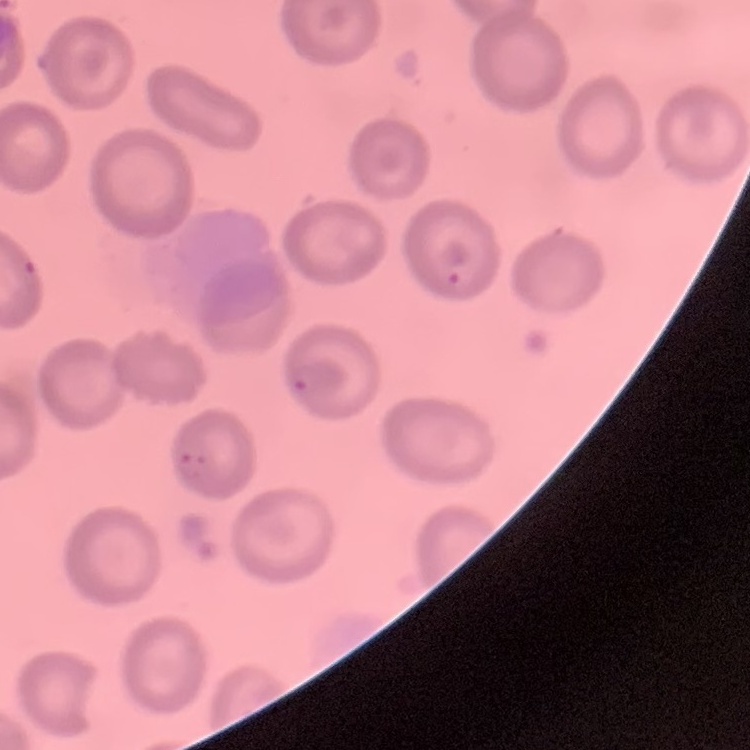
red blood cell morphology = no rouleaux formation
image type = one tile cut from a larger photomicrograph
preparation = thin blood film
stain = Field's or Giemsa